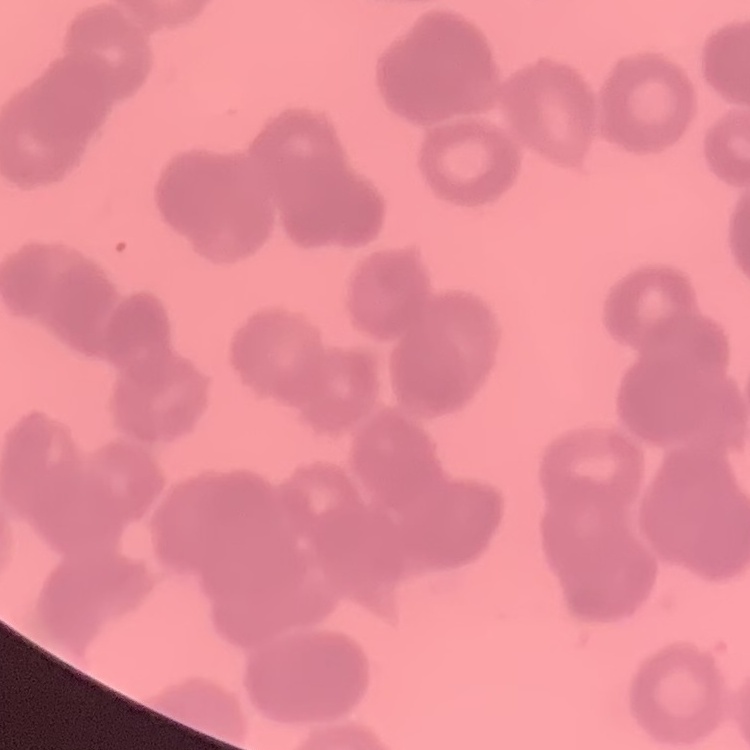
Summary:
  - Red blood cell morphology: rouleaux formation
  - Preparation: thin blood smear
  - Stain: Field's or Giemsa
  - Image type: square crop of a larger photomicrograph